Give the preparation type.
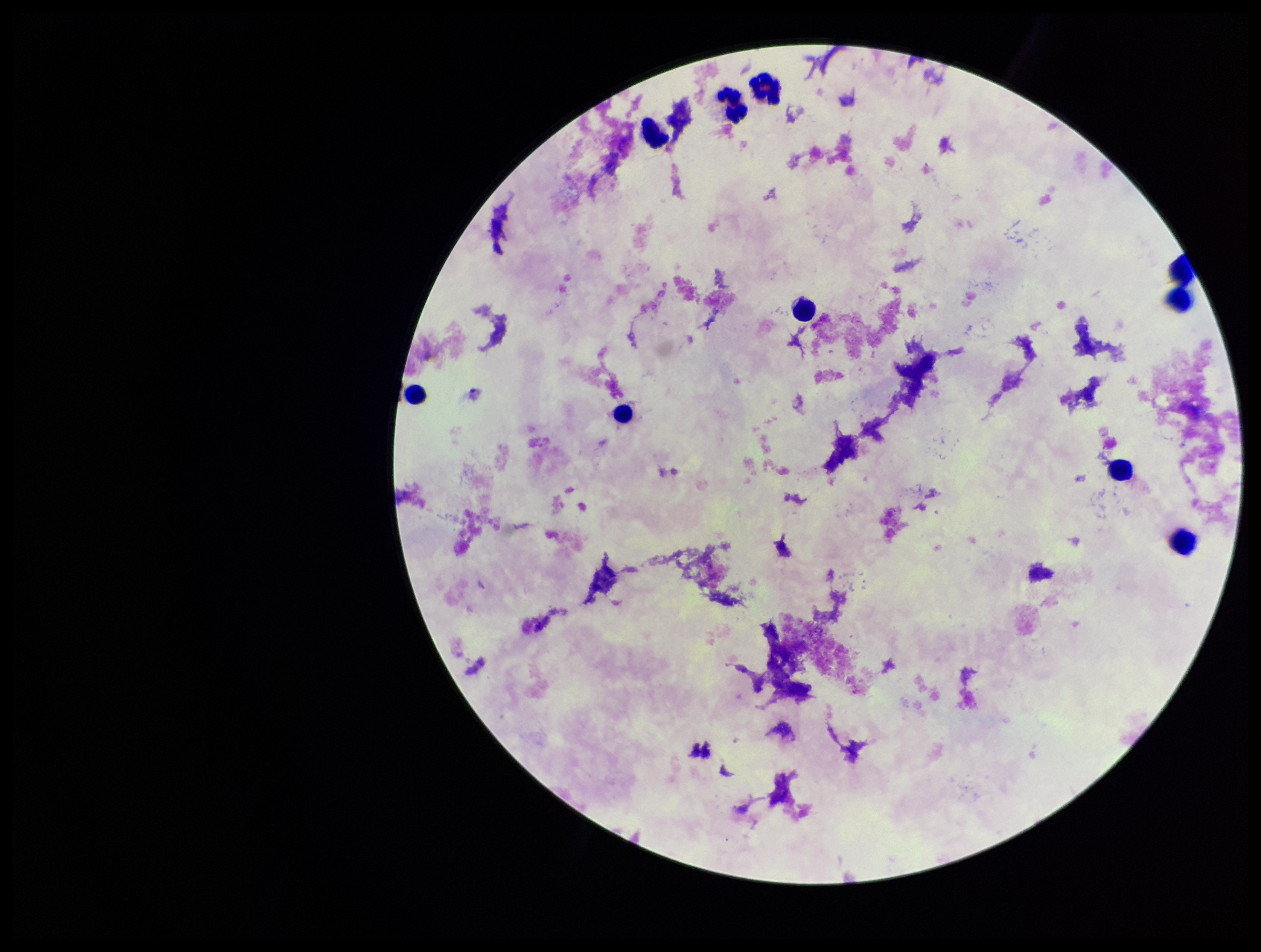
It is a thick blood smear.

Summary:
  - Plasmodium parasites: none detected
  - Field of view: one from this slide
  - Leukocyte count: 10
  - Parasite count: 0
  - Capture: smartphone photograph through the microscope eyepiece
  - Patient malaria status: negative
  - Stain: Giemsa
  - Image size: 1261×952 pixels